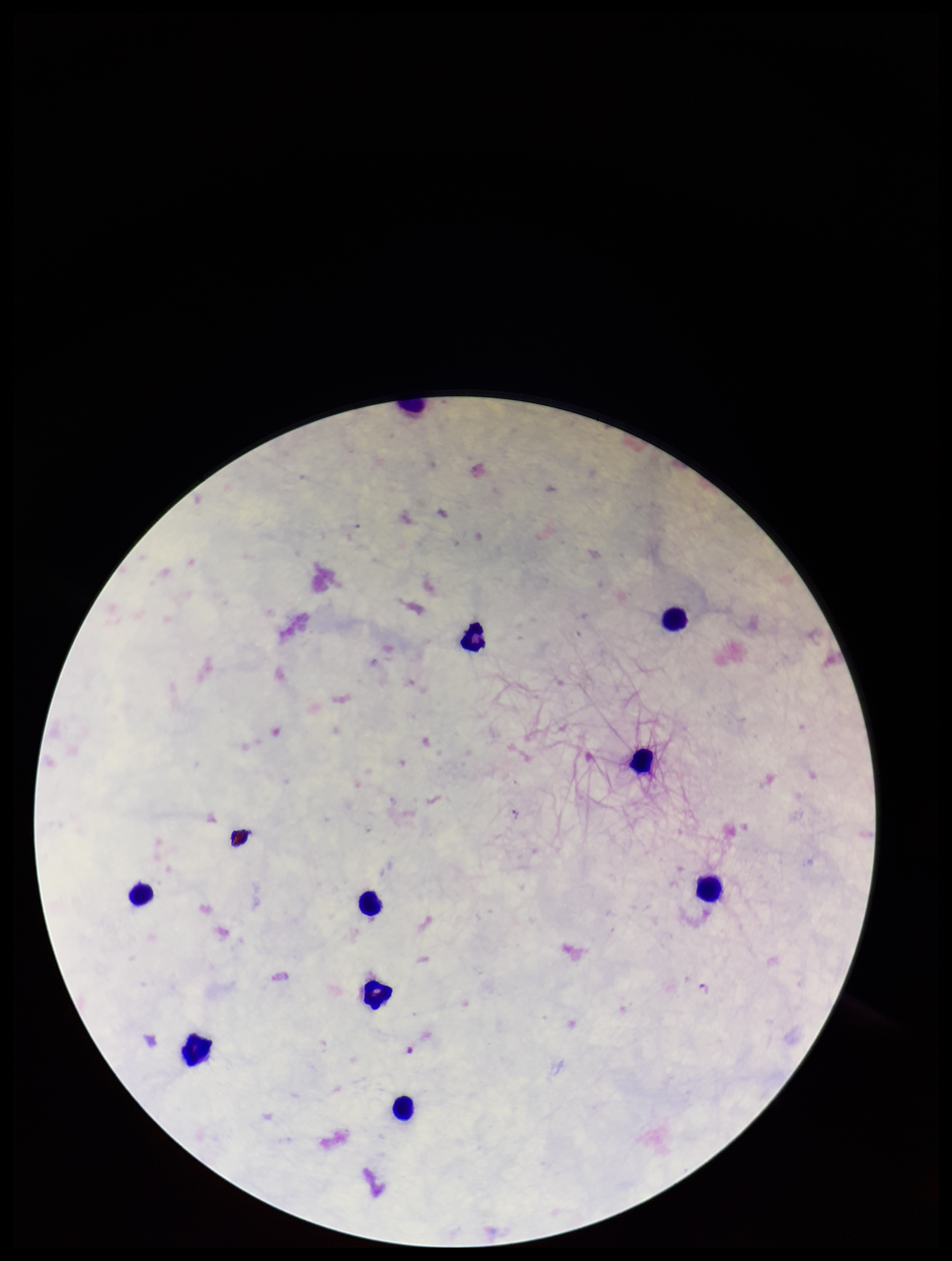
Photographed through the microscope eyepiece with a smartphone camera. Plasmodium parasites: none seen. Parasite count: 0. Single field of view. Image is 952×1261 pixels. Patient malaria status: negative. Preparation: thick smear. Giemsa stain. Leukocyte count: 9.